Locate every malaria parasite by life-cycle stage, and every leukocyte.
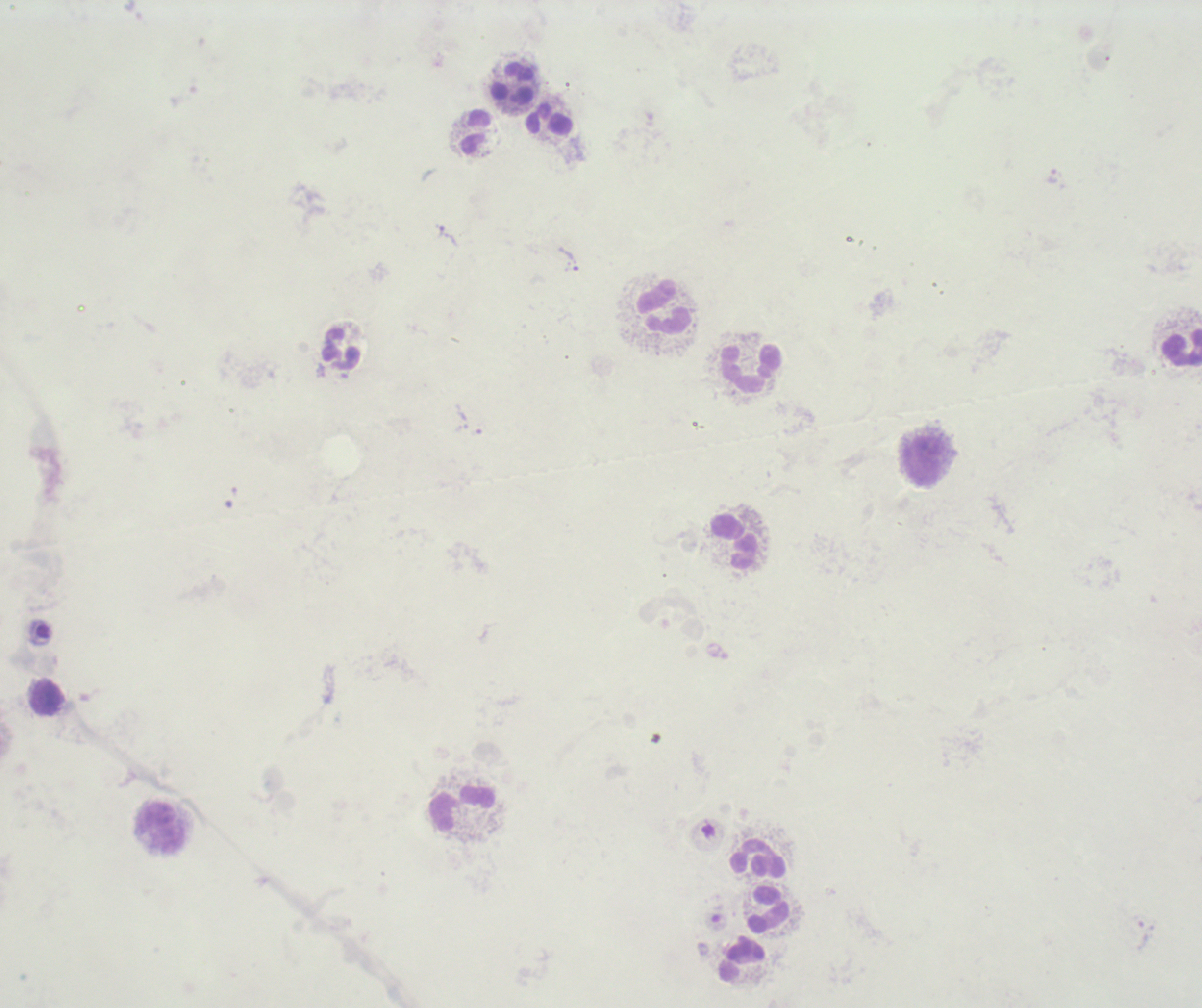
Approximate centers as [x, y] in pixels.
Trophozoites: [441, 232], [569, 259].
No schizont or gametocyte forms observed.
Leukocytes: [514, 82], [549, 120], [476, 131], [663, 307], [1181, 348], [342, 349], [751, 368], [923, 461], [732, 542], [46, 696], [462, 808], [159, 828], [758, 859], [767, 908], [741, 959].

preparation: thick blood smear
image_size: 1202×1008 pixels
field_of_view: single
context: previously used in an actual diagnosis
stain: Romanowsky
magnification: 100x
background_quality: unsatisfactory